Comment on the morphology of the red blood cells.
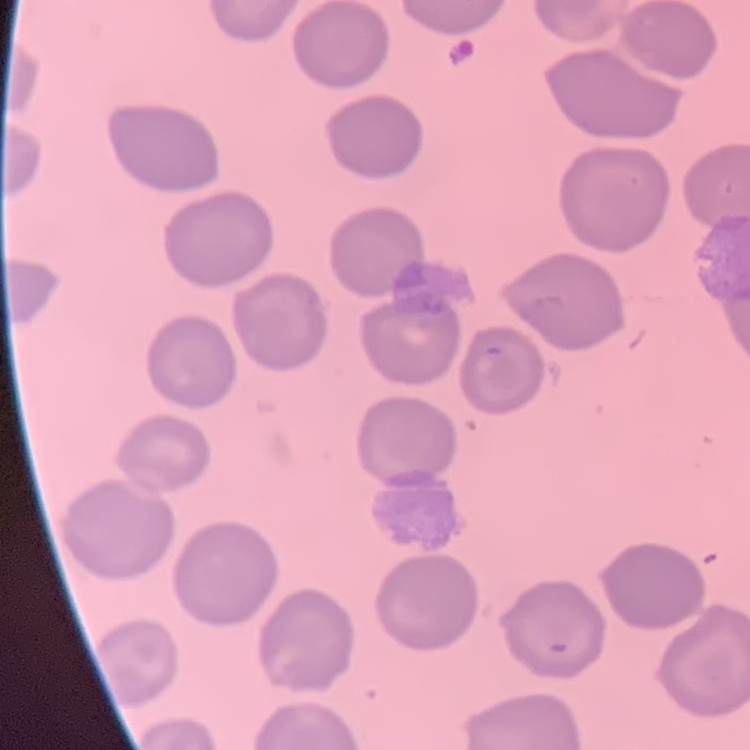

They show no rouleaux formation.

Summary:
  - Image type: one tile cut from a larger photomicrograph
  - Preparation: thin blood smear
  - Stain: Field's or Giemsa